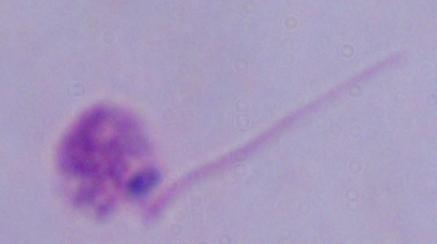
modality: photomicrograph
identification: Leishmania
magnification: 1000x